Locate every Plasmodium parasite.
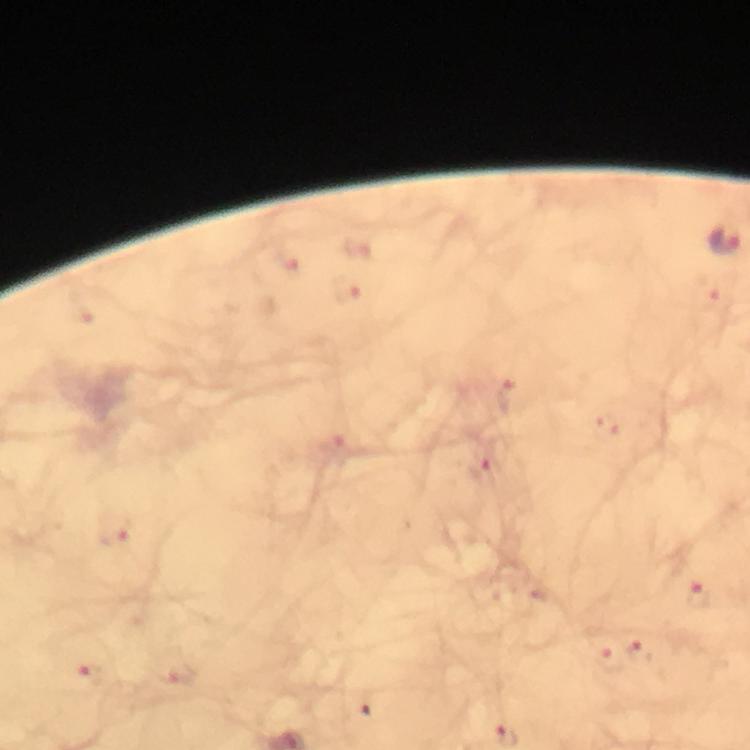

Approximate centers as {x, y} in pixels.
Plasmodium parasites: {724, 240}, {361, 246}, {290, 259}, {348, 293}, {714, 295}, {509, 398}, {334, 447}, {479, 465}, {115, 530}, {700, 594}, {640, 648}, {612, 662}, {91, 675}, {177, 678}.

{
  "image_size": "750×750 pixels",
  "capture": "smartphone photograph through a microscope",
  "stain": "Giemsa",
  "magnification": "100x",
  "cropped_from": "a single field of view",
  "immersion_oil": "applied",
  "preparation": "thick blood film",
  "context": "from a malaria diagnostic workup"
}